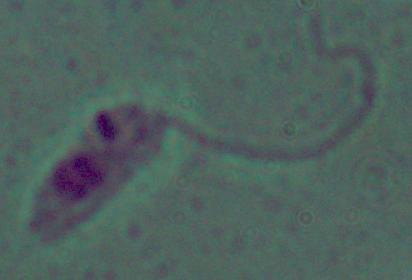
modality: photomicrograph
identification: Leishmania
magnification: 1000x